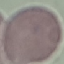
{
  "result": "negative for malaria parasites",
  "image_type": "cell patch, automatically extracted from a larger field of view and resized to 64 × 64 pixels",
  "preparation": "thin blood smear",
  "stain": "Giemsa",
  "capture": "smartphone camera at the microscope eyepiece"
}